Report the malaria status of this cell.
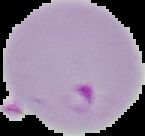

It is parasitized.

{
  "image_size": "145×136 pixels",
  "preparation": "thin blood film",
  "image_type": "cell region segmented out of the field of view; surrounding area masked to black"
}